Describe the morphology of the red blood cells.
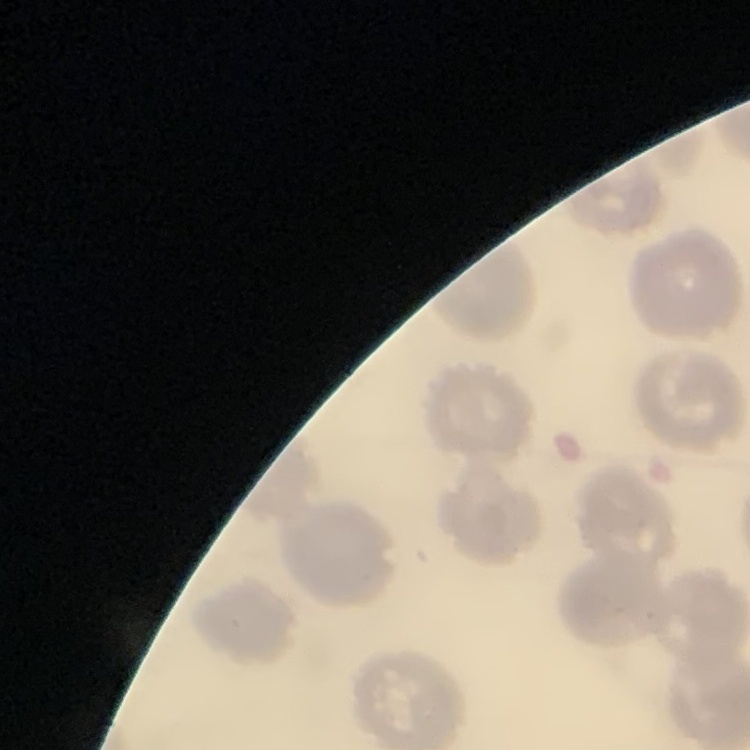

They show no rouleaux formation.

Square crop of a larger photomicrograph. Thin blood film. Field's or Giemsa stain.